Give the preparation type.
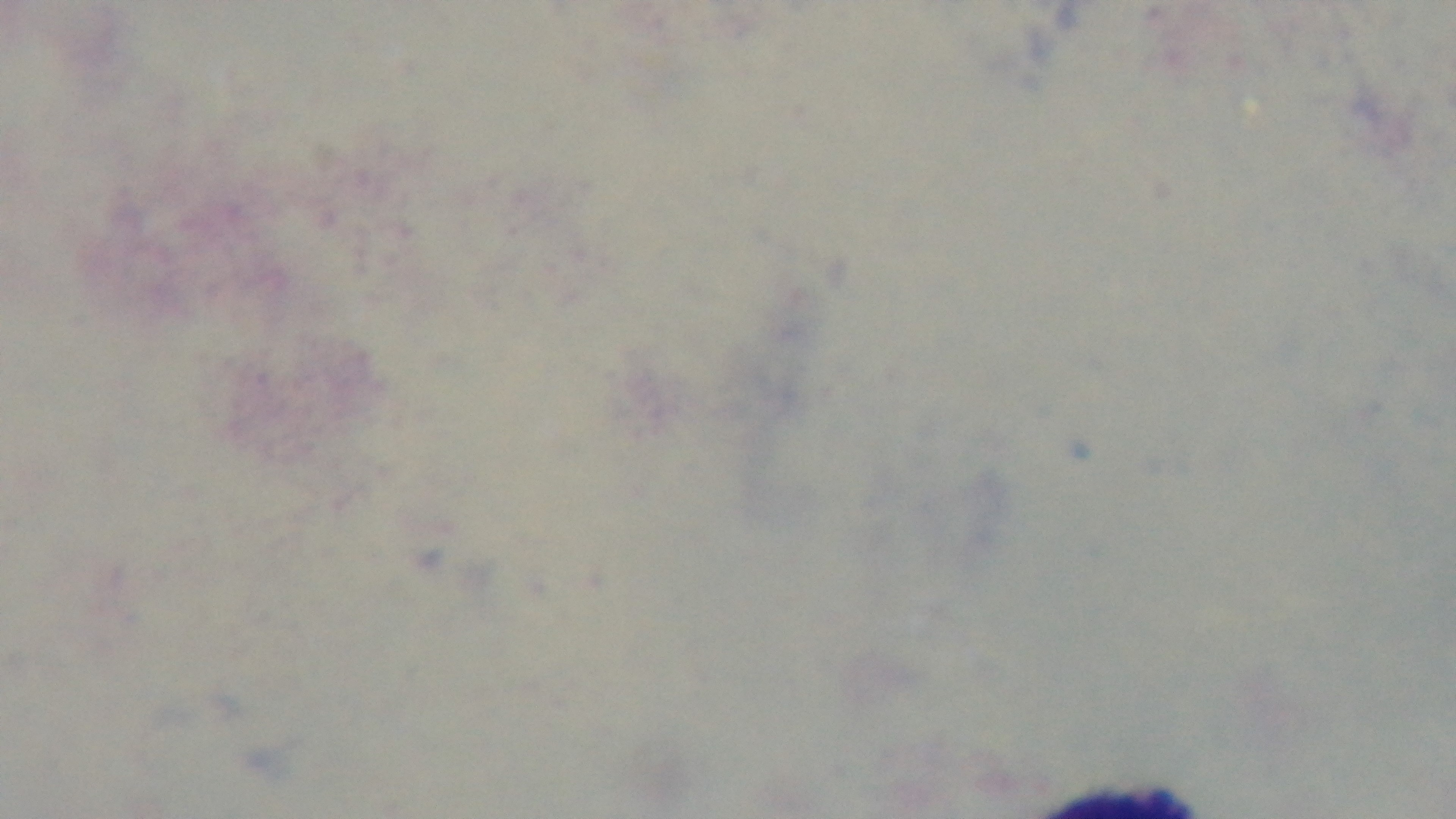

Thick.

Summary:
  - Modality: light microscopy
  - Objective: 100x oil immersion
  - Stain: Giemsa
  - Field of view: single
  - Malaria status: negative
  - Capture: mounted 4K digital camera